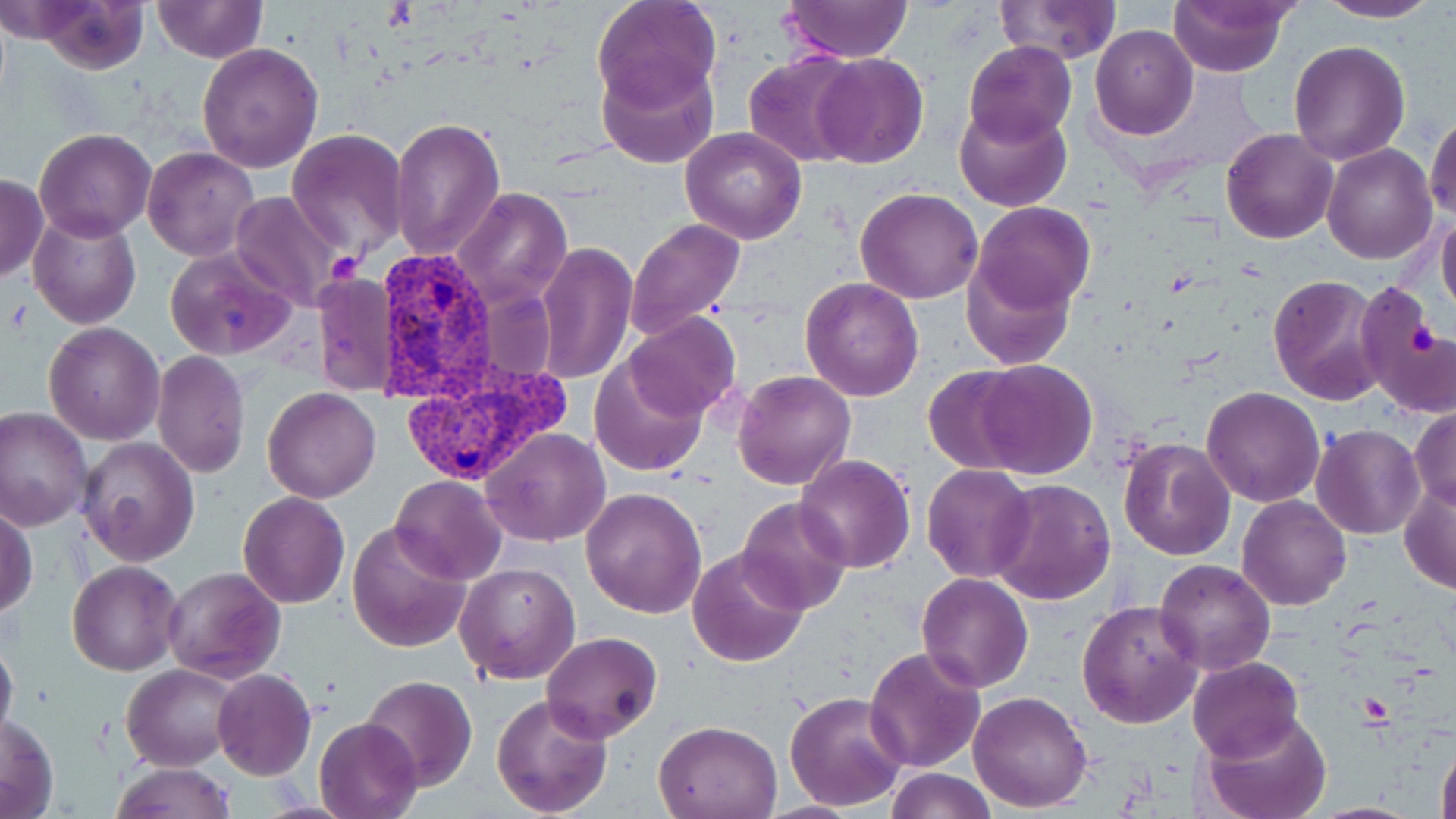

Approximate bounding boxes as (x1,y1)-(x2,y2) corner pairs in pixels. Platelet locations: (326,252)-(362,285), (1408,321)-(1439,357). Plasmodium vivax-infected red blood cell locations: (375,252)-(503,405), (397,360)-(571,488). Uninfected red blood cell locations: (26,0)-(151,72), (593,0)-(721,112), (778,0)-(913,65), (994,0)-(1121,65), (1168,0)-(1296,76), (1317,0)-(1443,23), (151,2)-(268,64), (1090,24)-(1197,139), (1288,40)-(1410,166), (964,41)-(1077,148), (197,42)-(324,173), (745,52)-(864,168), (810,53)-(929,168), (597,58)-(719,170), (954,102)-(1073,213), (1426,110)-(1456,221), (389,115)-(505,261), (679,127)-(806,244), (34,128)-(157,242), (287,129)-(408,255), (1221,129)-(1338,244), (1321,144)-(1436,264), (142,147)-(260,262), (0,173)-(48,283), (453,187)-(573,307), (854,187)-(983,303), (231,191)-(347,312), (972,201)-(1096,318), (28,211)-(141,329), (1438,211)-(1456,318), (626,218)-(745,339), (535,241)-(637,385), (164,244)-(298,361), (963,253)-(1078,370), (313,272)-(395,396), (1268,274)-(1385,405), (800,278)-(925,402), (1355,283)-(1455,420), (623,312)-(742,423), (44,322)-(164,444), (151,350)-(251,478), (591,355)-(709,479), (972,359)-(1098,478), (922,366)-(1033,473), (733,370)-(856,490), (262,385)-(381,503), (1202,387)-(1325,508), (1410,405)-(1456,510), (1,408)-(93,531), (1312,424)-(1426,540), (482,427)-(609,547), (1117,435)-(1235,559), (76,437)-(200,567), (795,453)-(917,573), (922,463)-(1036,582), (391,475)-(504,583), (990,478)-(1114,605), (1399,479)-(1456,597), (580,486)-(707,619), (238,492)-(351,609), (1237,495)-(1352,610), (737,496)-(852,617), (1,505)-(38,618), (347,521)-(473,653), (687,546)-(810,668), (1154,558)-(1274,675), (68,561)-(182,675), (455,562)-(580,684), (163,567)-(286,683), (917,573)-(1034,693), (887,593)-(1020,756), (1076,599)-(1203,729), (541,631)-(662,743), (0,635)-(18,744), (864,645)-(985,773), (1187,655)-(1303,761), (122,663)-(242,770), (211,669)-(316,780), (362,676)-(478,790), (783,690)-(907,810), (968,691)-(1093,811), (491,692)-(613,816), (1,711)-(59,816), (1200,711)-(1332,819), (315,715)-(422,819), (654,717)-(783,819), (1433,732)-(1456,819), (108,763)-(236,818), (887,768)-(999,818), (756,801)-(868,819). Slide-level diagnosis: Plasmodium vivax. Light microscopy. 1000x magnification. Thin blood film. Image is 1456×819 pixels. One field of a larger specimen. May-Grünwald-Giemsa stain.